State the blood parasite species.
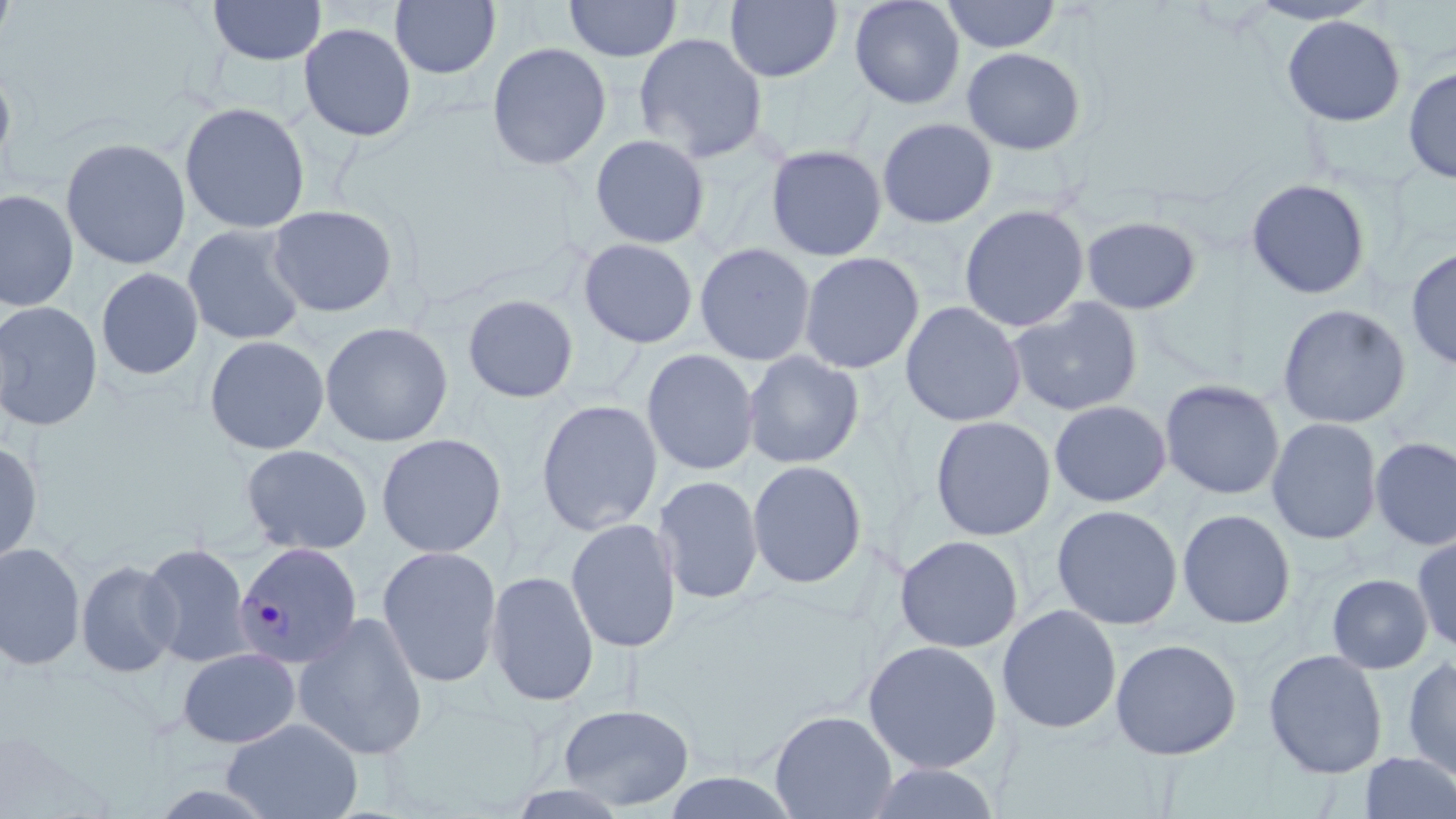

Plasmodium malariae.

Summary:
  - Coordinate format: approximate bounding boxes as (x1,y1)-(x2,y2) corner pairs in pixels
  - Uninfected red blood cell locations: (0,0)-(18,56), (208,0)-(326,66), (389,0)-(501,80), (564,0)-(682,62), (725,0)-(842,83), (848,0)-(966,110), (940,0)-(1062,55), (1242,0)-(1383,26), (1281,15)-(1406,127), (298,21)-(417,143), (633,31)-(768,164), (486,41)-(612,171), (961,46)-(1086,156), (0,60)-(17,179), (1402,66)-(1456,186), (179,101)-(310,234), (877,117)-(998,229), (589,134)-(711,250), (60,137)-(192,270), (765,143)-(888,262), (1245,178)-(1372,300), (0,188)-(79,313), (266,204)-(398,317), (959,204)-(1090,332), (1080,216)-(1202,315), (182,223)-(308,347), (577,237)-(700,349), (695,242)-(817,366), (1405,247)-(1456,373), (798,251)-(925,375), (95,266)-(204,381), (462,293)-(579,404), (1007,296)-(1144,417), (0,300)-(103,432), (900,301)-(1027,427), (1276,303)-(1412,429), (319,321)-(454,447), (203,334)-(330,455), (641,348)-(760,476), (742,350)-(865,470), (1159,379)-(1286,500), (535,399)-(663,536), (1048,399)-(1172,507), (929,415)-(1056,542), (1266,417)-(1383,545), (375,433)-(507,558), (1369,436)-(1456,551), (0,440)-(43,566), (240,443)-(373,556), (747,459)-(868,589), (652,473)-(763,605), (1051,503)-(1183,630), (1177,508)-(1297,630), (565,518)-(682,654), (1412,533)-(1456,653), (894,534)-(1024,653), (0,541)-(86,671), (140,541)-(251,668), (377,545)-(503,687), (75,558)-(181,678), (486,570)-(599,707), (1327,573)-(1433,674), (997,604)-(1122,735), (292,612)-(430,760), (996,615)-(1241,746), (862,638)-(1003,773), (1110,638)-(1242,760), (177,646)-(301,748), (1263,649)-(1388,779), (1402,655)-(1456,780), (557,703)-(695,811), (769,709)-(898,819), (221,717)-(364,819), (1357,751)-(1456,819), (862,762)-(1003,819)
  - Plasmodium malariae-infected red blood cell locations: (234,541)-(363,670)
  - Stain: May-Grünwald-Giemsa
  - Modality: optical microscopy
  - Magnification: 1000x
  - Field of view: one of a larger specimen
  - Preparation: thin blood smear
  - Image size: 1456×819 pixels